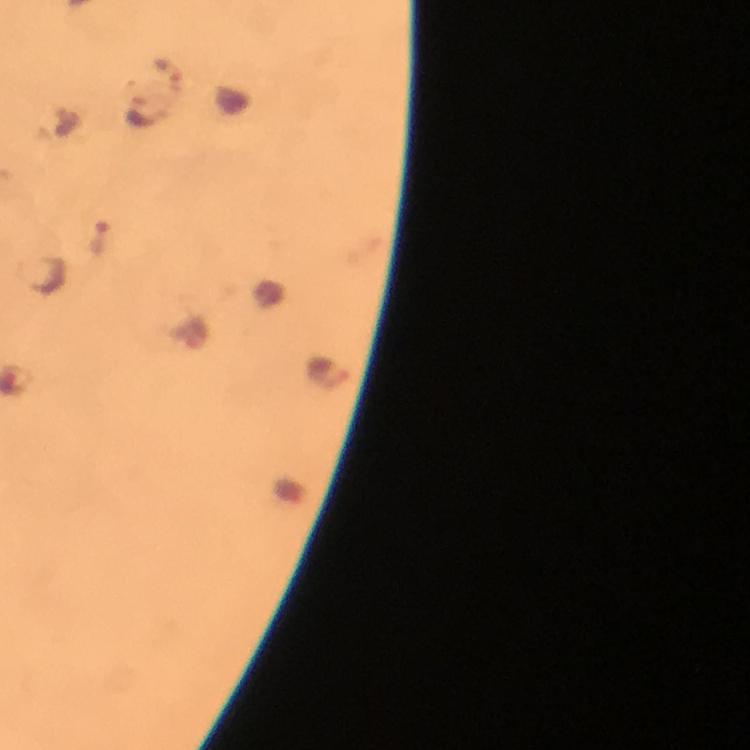

Approximate centers as {x, y} in pixels.
Summary:
  - Plasmodium parasite locations: {168, 69}, {143, 112}, {101, 240}, {327, 371}
  - Immersion oil: applied
  - Context: from a malaria diagnostic workup
  - Stain: Giemsa
  - Cropped from: one field of view
  - Preparation: thick blood film
  - Magnification: 100x
  - Image size: 750×750 pixels
  - Capture: smartphone camera through the microscope